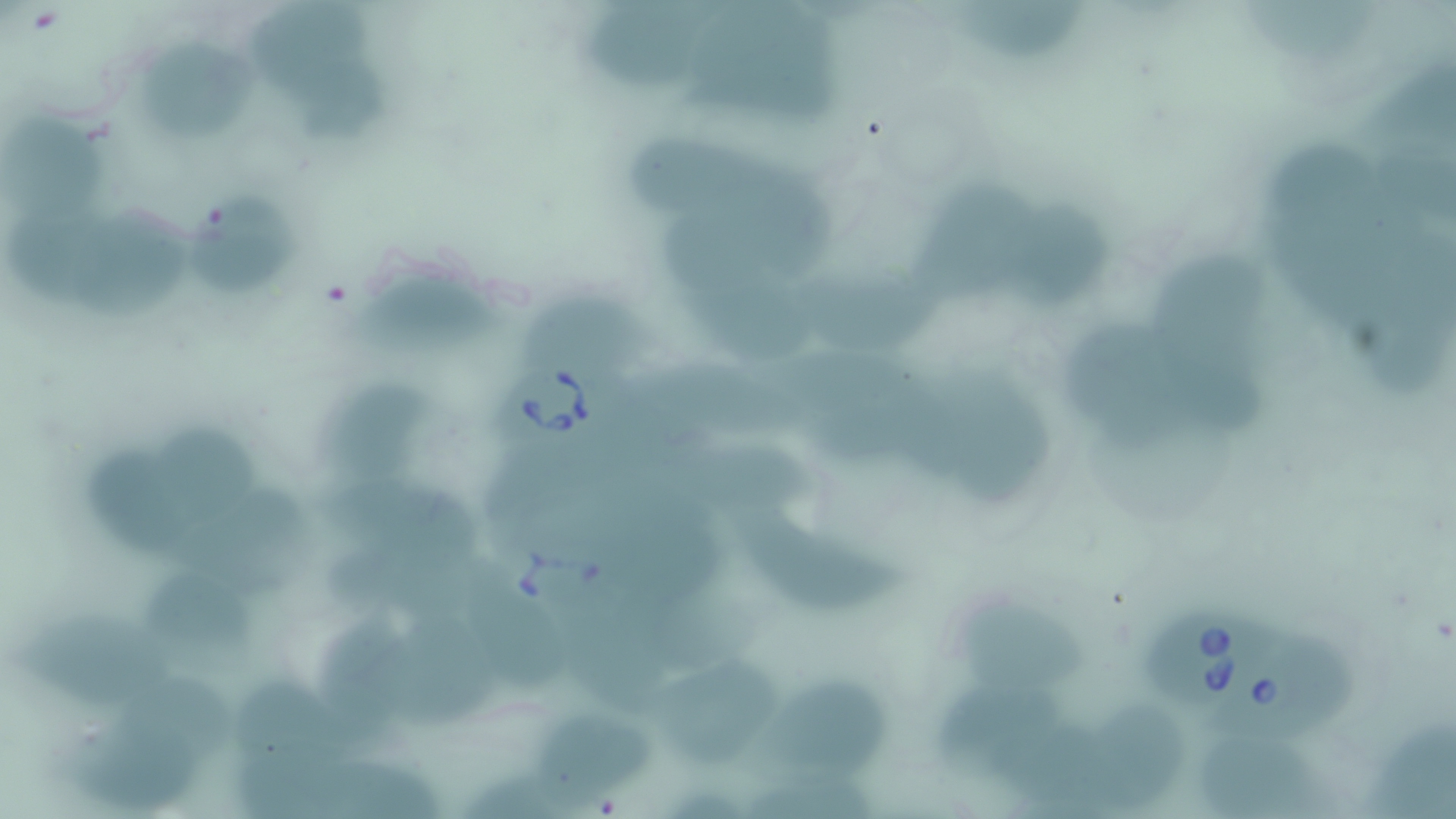 Approximate bounding boxes as (x1,y1)-(x2,y2) corner pairs in pixels. Babesia divergens-infected red blood cell locations: (503,360)-(626,463), (501,522)-(627,629), (1141,604)-(1291,708), (1215,632)-(1361,745). Uninfected red blood cell locations: (257,0)-(369,97), (586,0)-(704,94), (704,3)-(845,128), (1249,5)-(1384,58), (969,6)-(1094,66), (146,39)-(260,141), (1374,56)-(1456,145), (306,57)-(391,141), (3,102)-(110,222), (1381,124)-(1456,212), (626,135)-(767,208), (1271,144)-(1393,226), (936,163)-(1074,300), (751,170)-(847,270), (190,190)-(303,302), (1260,192)-(1385,300), (1022,196)-(1114,298), (1355,198)-(1456,292), (84,203)-(185,313), (12,206)-(133,298), (669,220)-(767,302), (1168,253)-(1270,338), (354,274)-(520,353), (799,275)-(952,352), (1363,286)-(1456,404), (520,294)-(657,363), (706,295)-(822,363), (1074,322)-(1168,447), (1172,349)-(1271,443), (783,356)-(932,418), (647,368)-(814,428), (944,372)-(1063,511), (342,381)-(437,469), (823,393)-(965,475), (170,419)-(261,530), (670,443)-(823,502), (91,447)-(201,557), (483,462)-(625,532), (330,473)-(481,561), (197,487)-(311,582), (752,513)-(908,616), (627,525)-(729,617), (324,534)-(477,612), (143,561)-(252,647), (471,568)-(564,686), (405,602)-(500,721), (968,602)-(1091,688), (328,603)-(421,729), (20,616)-(173,698), (572,617)-(686,711), (650,666)-(784,755), (122,671)-(237,751), (759,680)-(894,766), (235,682)-(357,747), (933,682)-(1067,763), (1097,703)-(1184,798), (538,708)-(660,804), (1000,722)-(1098,796), (1205,722)-(1327,817), (1369,723)-(1456,819), (75,731)-(201,805), (241,737)-(326,817), (323,754)-(446,816), (763,762)-(886,818). Slide-level diagnosis: Babesia divergens. Light microscopy. 1000x magnification. Thin blood smear. Image is 1456×819 pixels. One field of a larger specimen. May-Grünwald-Giemsa stain.